Evaluate for parasitized red blood cells.
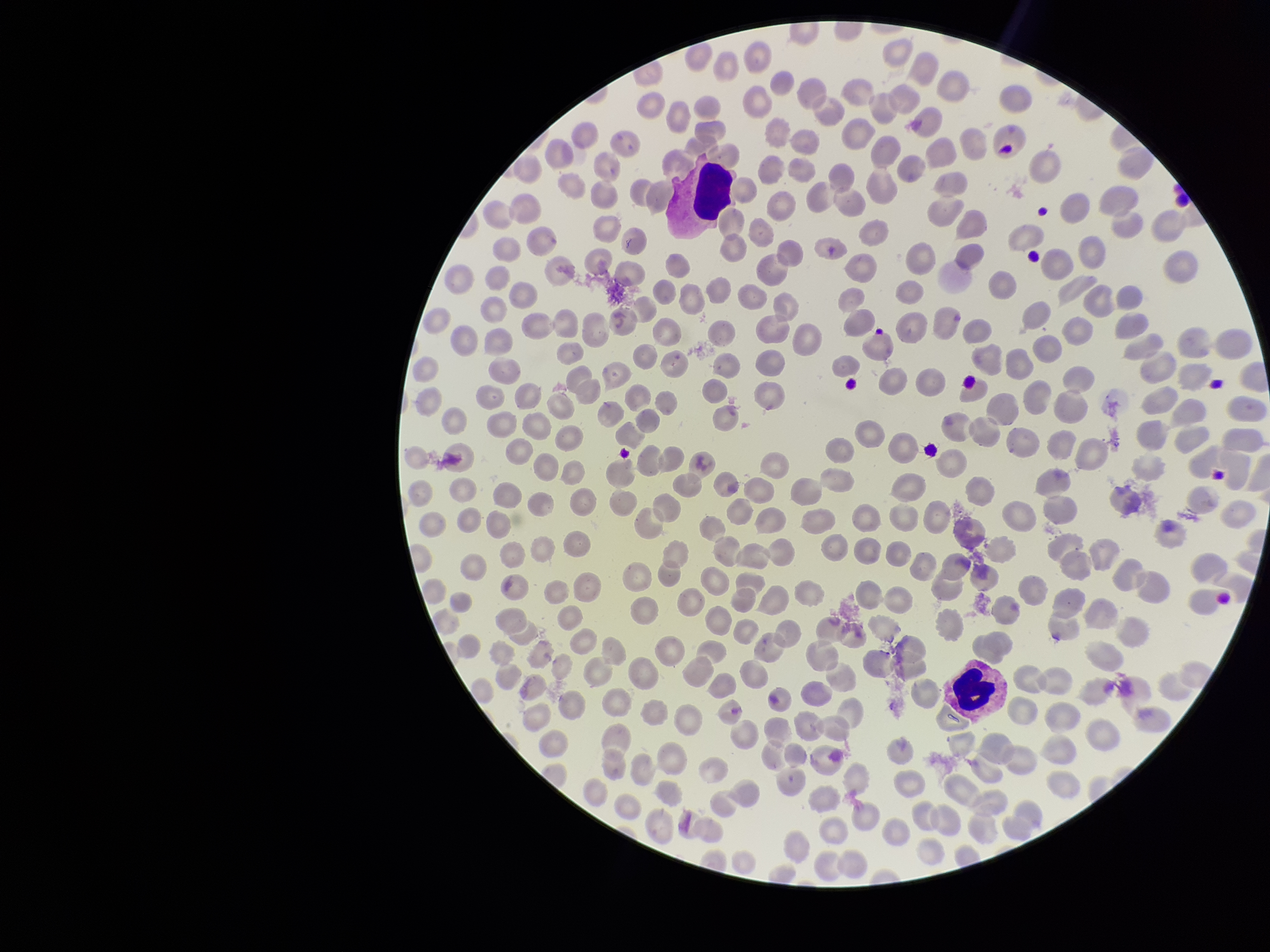

None seen.

Smartphone photograph taken through the eyepiece of a microscope. Red blood cell count: 240. Species reported for this patient: Plasmodium falciparum. Giemsa stain. Patient malaria status: infected. Preparation: thin blood smear. Image is 1270×952 pixels. Parasitized red blood cell count: 0. One field from this slide.